Outline platelets.
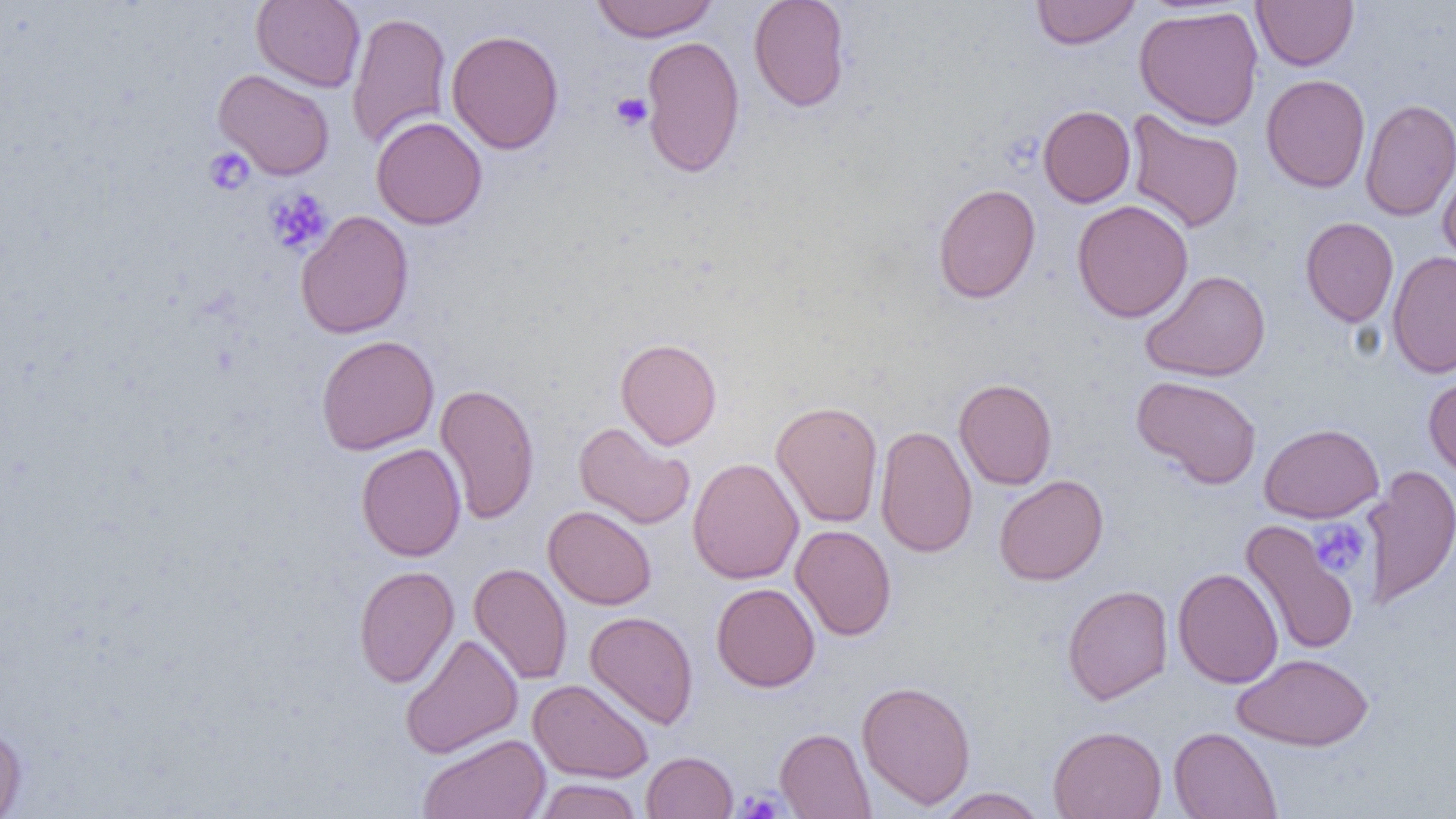

Approximate bounding boxes as named x1/y1/x2/y2 corners in pixels.
Platelets: (x1=610, y1=92, x2=653, y2=131), (x1=203, y1=147, x2=254, y2=196), (x1=265, y1=188, x2=333, y2=255), (x1=1309, y1=520, x2=1370, y2=577), (x1=737, y1=788, x2=787, y2=818).

Summary:
  - Uninfected red blood cell locations: (x1=251, y1=0, x2=366, y2=92), (x1=590, y1=0, x2=719, y2=42), (x1=749, y1=0, x2=851, y2=112), (x1=1030, y1=0, x2=1141, y2=49), (x1=1252, y1=0, x2=1359, y2=71), (x1=1134, y1=5, x2=1263, y2=130), (x1=347, y1=10, x2=453, y2=149), (x1=446, y1=29, x2=564, y2=154), (x1=640, y1=34, x2=746, y2=178), (x1=212, y1=68, x2=335, y2=180), (x1=1260, y1=74, x2=1370, y2=192), (x1=1360, y1=98, x2=1456, y2=222), (x1=1038, y1=105, x2=1136, y2=208), (x1=1126, y1=109, x2=1244, y2=233), (x1=371, y1=116, x2=487, y2=230), (x1=1438, y1=161, x2=1456, y2=273), (x1=933, y1=183, x2=1041, y2=304), (x1=1072, y1=199, x2=1193, y2=323), (x1=295, y1=210, x2=413, y2=339), (x1=1300, y1=217, x2=1399, y2=327), (x1=1387, y1=250, x2=1456, y2=378), (x1=1141, y1=269, x2=1270, y2=381), (x1=316, y1=335, x2=439, y2=455), (x1=615, y1=338, x2=722, y2=450), (x1=1423, y1=367, x2=1456, y2=482), (x1=1131, y1=375, x2=1262, y2=489), (x1=953, y1=378, x2=1058, y2=490), (x1=434, y1=383, x2=540, y2=524), (x1=771, y1=400, x2=883, y2=528), (x1=573, y1=422, x2=695, y2=529), (x1=1259, y1=423, x2=1384, y2=522), (x1=875, y1=424, x2=977, y2=558), (x1=355, y1=442, x2=466, y2=561), (x1=687, y1=457, x2=804, y2=584), (x1=1361, y1=465, x2=1456, y2=610), (x1=993, y1=474, x2=1108, y2=586), (x1=543, y1=505, x2=657, y2=609), (x1=1241, y1=521, x2=1359, y2=656), (x1=790, y1=524, x2=897, y2=641), (x1=468, y1=562, x2=572, y2=684), (x1=353, y1=565, x2=459, y2=688), (x1=1172, y1=567, x2=1284, y2=688), (x1=711, y1=582, x2=821, y2=692), (x1=1062, y1=584, x2=1173, y2=705), (x1=584, y1=611, x2=698, y2=729), (x1=400, y1=633, x2=523, y2=759), (x1=1234, y1=653, x2=1373, y2=751), (x1=528, y1=679, x2=653, y2=783), (x1=857, y1=680, x2=976, y2=810), (x1=0, y1=723, x2=27, y2=818), (x1=1048, y1=725, x2=1167, y2=819), (x1=1168, y1=726, x2=1282, y2=819), (x1=774, y1=727, x2=876, y2=819), (x1=418, y1=733, x2=551, y2=819), (x1=641, y1=751, x2=738, y2=818), (x1=534, y1=779, x2=643, y2=819), (x1=934, y1=787, x2=1048, y2=819)
  - Slide-level diagnosis: negative for blood parasites
  - Magnification: 1000x
  - Field of view: single
  - Modality: optical microscopy
  - Image size: 1456×819 pixels
  - Preparation: thin blood smear